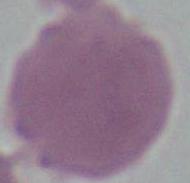

{
  "modality": "micrograph",
  "identification": "erythrocyte",
  "magnification": "1000x"
}